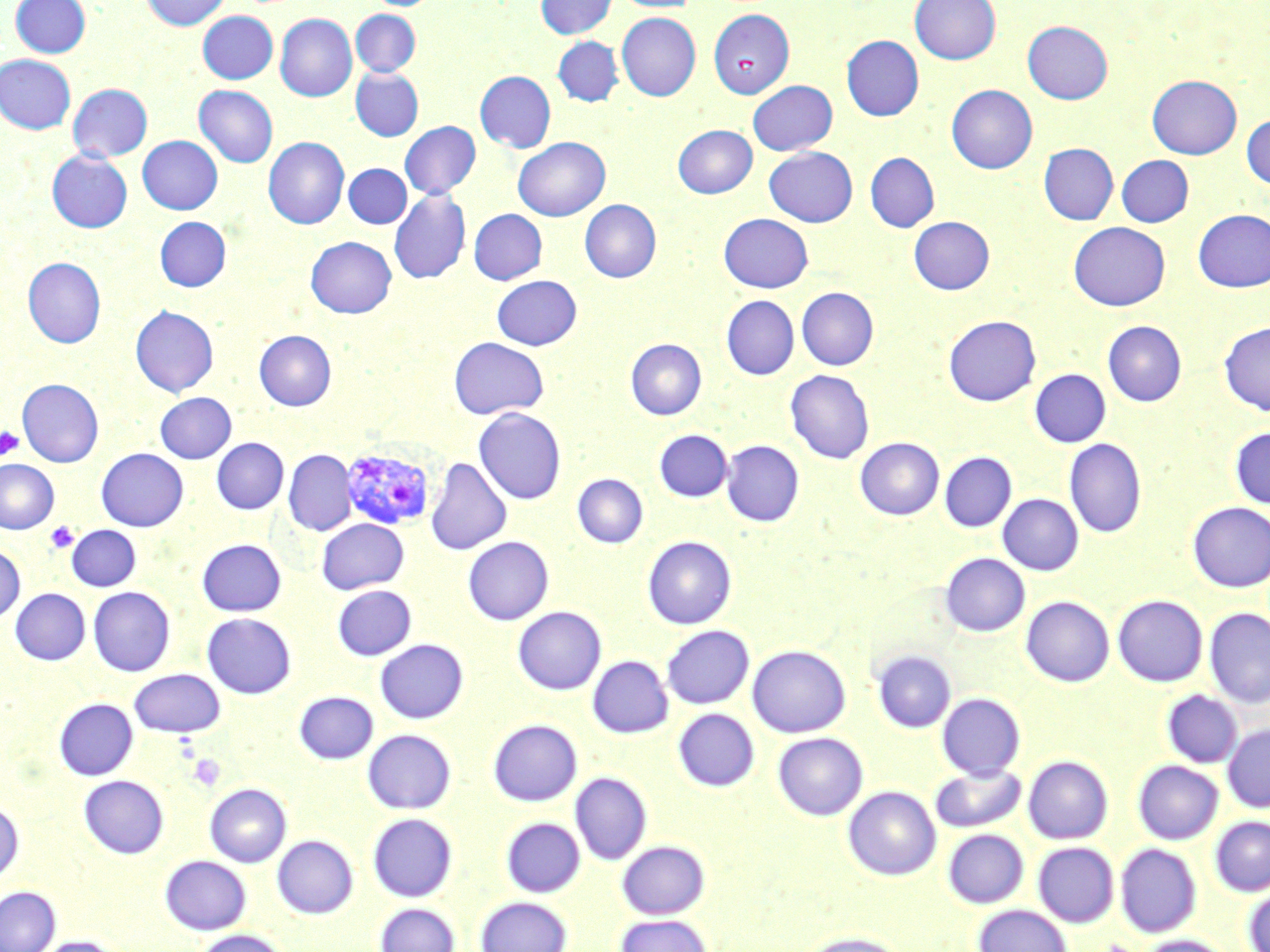

slide_level_diagnosis: Plasmodium vivax
uninfected_red_blood_cell_locations: 'approximate bounding boxes as [x1, y1, x2, y2] in pixels: [10, 0, 91, 57], [141, 0, 230, 30], [368, 0, 438, 9], [535, 0, 616, 39], [611, 0, 700, 13], [910, 0, 1000, 65], [351, 9, 420, 76], [709, 9, 795, 98], [198, 11, 277, 84], [617, 12, 700, 100], [275, 13, 357, 101], [1022, 21, 1113, 104], [841, 35, 924, 121], [553, 37, 623, 105], [0, 55, 75, 133], [351, 68, 423, 141], [475, 71, 556, 153], [1147, 75, 1241, 159], [748, 80, 837, 155], [68, 84, 152, 162], [194, 85, 278, 167], [946, 85, 1037, 174], [1241, 114, 1270, 189], [400, 121, 480, 199], [673, 125, 757, 197], [138, 136, 222, 214], [264, 137, 349, 228], [513, 137, 610, 221], [1039, 143, 1118, 224], [765, 147, 857, 227], [47, 150, 132, 233], [865, 153, 939, 232], [1116, 155, 1193, 226], [343, 164, 411, 228], [389, 189, 471, 284], [580, 200, 661, 282], [469, 209, 547, 284], [1193, 209, 1270, 292], [719, 213, 813, 292], [155, 217, 230, 291], [909, 217, 994, 294], [1069, 222, 1170, 310], [306, 236, 396, 318], [23, 257, 105, 347], [492, 275, 582, 350], [796, 288, 878, 370], [721, 295, 799, 380], [130, 305, 218, 397], [943, 315, 1040, 406], [1103, 321, 1186, 406], [1219, 321, 1270, 415], [254, 330, 336, 410], [449, 337, 549, 419], [625, 338, 706, 419], [785, 369, 874, 464], [1030, 369, 1110, 446], [17, 378, 103, 467], [155, 392, 236, 463], [474, 408, 567, 505], [1230, 427, 1270, 509], [654, 430, 732, 501], [212, 438, 288, 514], [855, 438, 944, 520], [1064, 439, 1147, 538], [721, 441, 804, 526], [96, 448, 187, 531], [283, 450, 356, 535], [940, 452, 1017, 531], [426, 458, 511, 555], [0, 459, 58, 533], [572, 474, 648, 548], [998, 494, 1083, 575], [1187, 501, 1270, 592], [317, 518, 408, 594], [67, 525, 141, 591], [643, 536, 736, 629], [463, 537, 553, 625], [198, 539, 286, 616], [0, 544, 25, 624], [940, 553, 1029, 636], [333, 585, 416, 660], [88, 587, 175, 676], [11, 588, 90, 665], [1112, 595, 1207, 686], [1021, 596, 1114, 686], [513, 607, 606, 694], [1204, 608, 1270, 707], [202, 613, 296, 698], [661, 625, 754, 709], [375, 639, 468, 723], [747, 644, 850, 737], [872, 650, 956, 732], [588, 655, 673, 738], [129, 669, 226, 737], [295, 691, 378, 764], [1162, 691, 1242, 767], [937, 693, 1025, 778], [54, 698, 137, 780], [674, 708, 758, 790], [488, 719, 582, 805], [1223, 724, 1270, 812], [363, 729, 456, 814], [773, 732, 868, 820], [1023, 755, 1112, 844], [1133, 760, 1223, 844], [930, 764, 1026, 833], [571, 772, 652, 864], [79, 775, 168, 858], [205, 783, 291, 867], [843, 786, 941, 880], [0, 799, 24, 887], [367, 813, 457, 901], [1210, 816, 1270, 896], [502, 817, 584, 897], [943, 829, 1028, 908], [272, 835, 358, 918], [617, 840, 709, 919], [1033, 842, 1118, 927], [1115, 843, 1201, 937], [160, 855, 251, 934], [1242, 883, 1270, 951], [0, 886, 60, 952], [476, 896, 572, 952], [375, 903, 459, 952], [973, 904, 1072, 952], [614, 913, 712, 952], [193, 929, 288, 952], [798, 932, 908, 952], [1136, 934, 1232, 952], [32, 936, 126, 952]'
plasmodium_vivax_infected_red_blood_cell_locations: 'approximate bounding boxes as [x1, y1, x2, y2] in pixels: [341, 447, 436, 531]'
platelet_locations: 'approximate bounding boxes as [x1, y1, x2, y2] in pixels: [0, 425, 24, 460], [46, 522, 79, 553], [187, 753, 226, 791]'
magnification: 1000x
image_size: 1270×952 pixels
modality: optical microscopy
stain: May-Grünwald-Giemsa
field_of_view: single
preparation: thin blood smear